Name the blood parasite species.
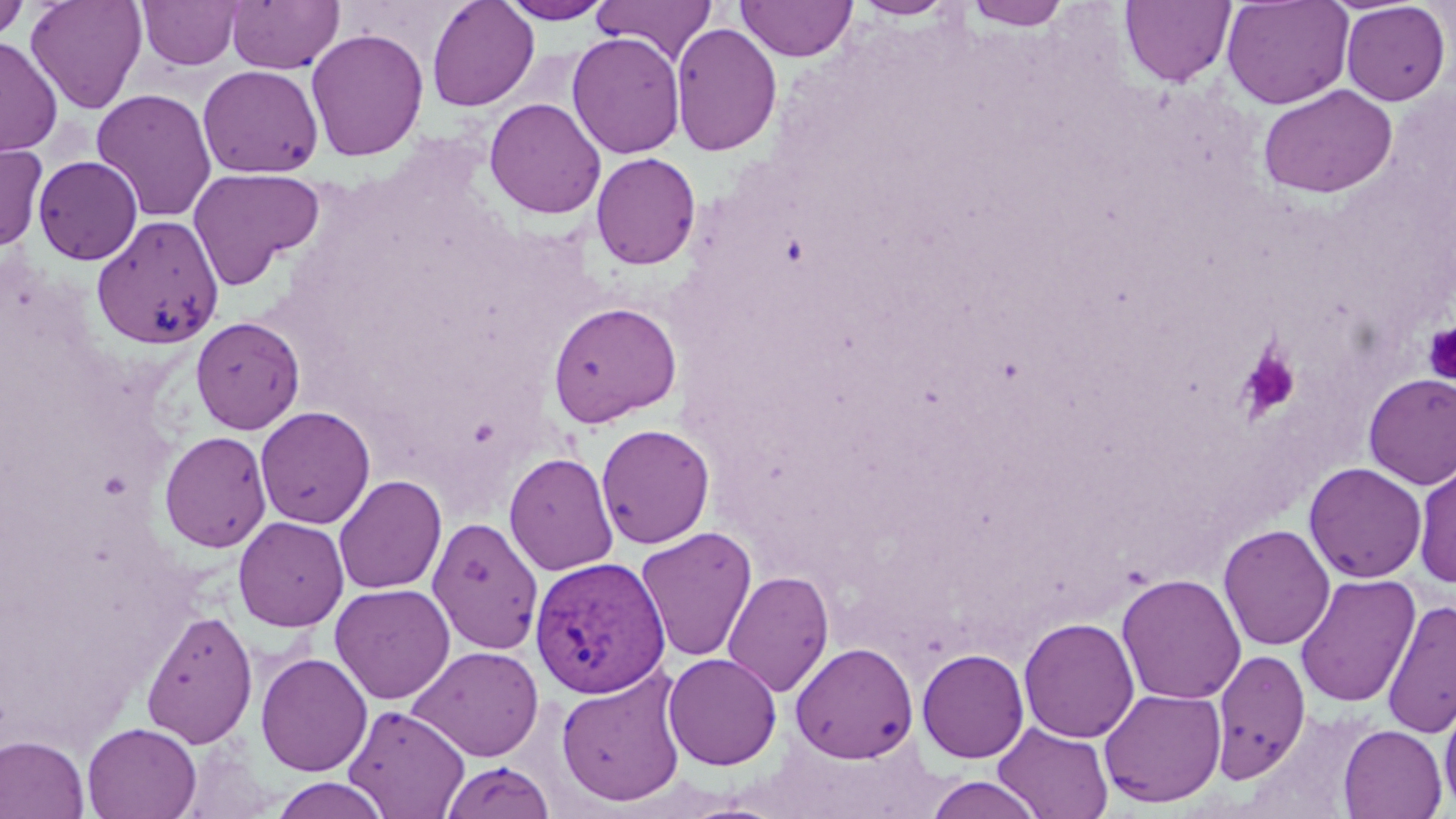
Plasmodium vivax.

magnification = 1000x
image size = 1456×819 pixels
preparation = thin blood smear
uninfected red blood cell locations = approximate bounding boxes as named x1/y1/x2/y2 corners in pixels: (x1=25, y1=0, x2=148, y2=114), (x1=135, y1=0, x2=245, y2=70), (x1=225, y1=0, x2=344, y2=73), (x1=426, y1=0, x2=539, y2=112), (x1=591, y1=0, x2=717, y2=64), (x1=852, y1=0, x2=959, y2=20), (x1=963, y1=0, x2=1072, y2=30), (x1=1120, y1=0, x2=1235, y2=87), (x1=1222, y1=0, x2=1354, y2=110), (x1=0, y1=1, x2=31, y2=44), (x1=499, y1=1, x2=613, y2=23), (x1=736, y1=1, x2=857, y2=62), (x1=1340, y1=2, x2=1451, y2=106), (x1=670, y1=22, x2=782, y2=157), (x1=305, y1=28, x2=429, y2=162), (x1=567, y1=32, x2=686, y2=159), (x1=0, y1=36, x2=63, y2=157), (x1=197, y1=64, x2=324, y2=178), (x1=1258, y1=84, x2=1398, y2=199), (x1=91, y1=88, x2=217, y2=222), (x1=484, y1=98, x2=606, y2=219), (x1=0, y1=141, x2=49, y2=253), (x1=591, y1=152, x2=701, y2=270), (x1=32, y1=155, x2=144, y2=265), (x1=188, y1=167, x2=324, y2=288), (x1=91, y1=215, x2=224, y2=349), (x1=547, y1=301, x2=682, y2=428), (x1=190, y1=316, x2=305, y2=434), (x1=1362, y1=373, x2=1456, y2=488), (x1=254, y1=406, x2=376, y2=529), (x1=595, y1=423, x2=716, y2=549), (x1=159, y1=430, x2=272, y2=552), (x1=503, y1=452, x2=619, y2=576), (x1=1413, y1=458, x2=1456, y2=588), (x1=1303, y1=461, x2=1427, y2=583), (x1=333, y1=474, x2=448, y2=595), (x1=233, y1=516, x2=349, y2=631), (x1=427, y1=516, x2=544, y2=654), (x1=1218, y1=524, x2=1336, y2=651), (x1=635, y1=526, x2=758, y2=663), (x1=722, y1=569, x2=835, y2=698), (x1=1116, y1=573, x2=1247, y2=705), (x1=1295, y1=573, x2=1421, y2=708), (x1=330, y1=583, x2=455, y2=704), (x1=1382, y1=599, x2=1456, y2=738), (x1=140, y1=609, x2=258, y2=748), (x1=1018, y1=616, x2=1140, y2=743), (x1=790, y1=642, x2=918, y2=763), (x1=408, y1=645, x2=545, y2=761), (x1=1211, y1=647, x2=1311, y2=783), (x1=917, y1=648, x2=1030, y2=763), (x1=255, y1=651, x2=373, y2=777), (x1=662, y1=652, x2=782, y2=770), (x1=555, y1=667, x2=688, y2=807), (x1=1099, y1=687, x2=1227, y2=808), (x1=1439, y1=694, x2=1456, y2=815), (x1=344, y1=703, x2=470, y2=817), (x1=81, y1=722, x2=202, y2=819), (x1=993, y1=722, x2=1114, y2=819), (x1=1338, y1=724, x2=1448, y2=818), (x1=0, y1=734, x2=91, y2=819), (x1=439, y1=759, x2=557, y2=819), (x1=923, y1=775, x2=1046, y2=818), (x1=268, y1=777, x2=392, y2=818)
platelet locations = approximate bounding boxes as named x1/y1/x2/y2 corners in pixels: (x1=1422, y1=323, x2=1456, y2=383), (x1=1238, y1=346, x2=1302, y2=419)
Plasmodium vivax-infected red blood cell locations = approximate bounding boxes as named x1/y1/x2/y2 corners in pixels: (x1=529, y1=555, x2=670, y2=698)
stain = May-Grünwald-Giemsa
field of view = one of a larger specimen
modality = optical microscopy